Assess for parasitized red blood cells.
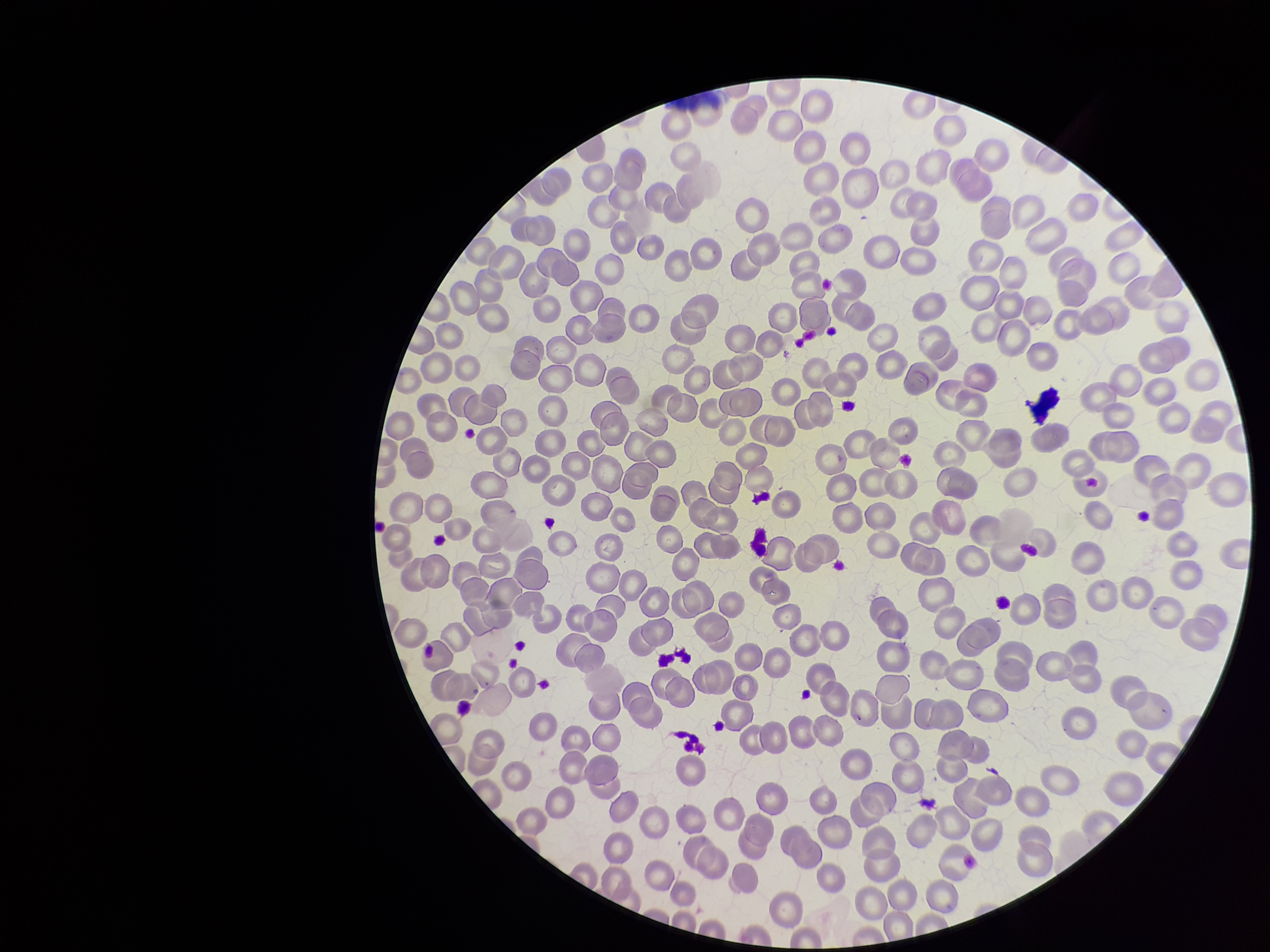
None seen.

Summary:
  - Capture: smartphone photograph through the microscope eyepiece
  - Preparation: thin blood smear
  - Patient malaria status: negative
  - Stain: Giemsa
  - Parasitized red blood cell count: 0
  - Image size: 1270×952 pixels
  - Field of view: single
  - Red blood cell count: 258